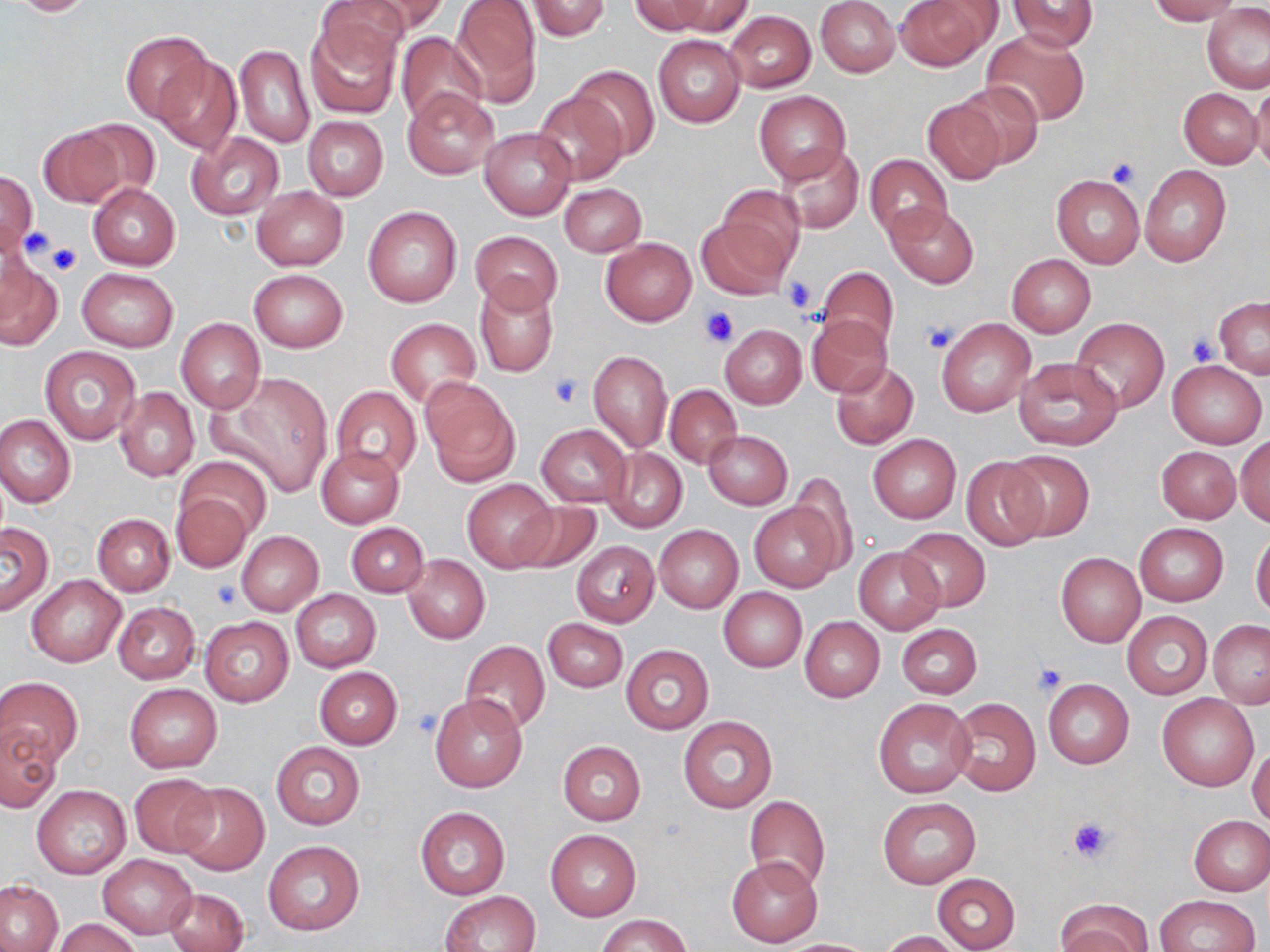
slide_level_diagnosis: no evidence of blood parasites
platelet_locations: 'approximate bounding boxes as (x1,y1)-(x2,y2) corner pairs in pixels: (1108,157)-(1141,188), (22,226)-(52,259), (47,242)-(83,276), (782,276)-(817,313), (701,306)-(740,346), (922,318)-(959,353), (1187,332)-(1219,366), (550,374)-(583,407), (213,581)-(241,609), (1033,662)-(1067,696), (411,707)-(445,737), (1066,815)-(1115,864)'
image_size: 1270×952 pixels
magnification: 1000x
uninfected_red_blood_cell_locations: 'approximate bounding boxes as (x1,y1)-(x2,y2) corner pairs in pixels: (5,0)-(101,17), (314,0)-(415,73), (351,0)-(449,41), (450,0)-(542,101), (631,0)-(712,36), (665,0)-(752,36), (816,0)-(900,77), (893,0)-(998,71), (1007,0)-(1102,52), (1148,0)-(1243,23), (526,1)-(610,41), (1202,4)-(1270,93), (725,11)-(815,93), (304,17)-(402,118), (983,29)-(1090,126), (121,30)-(212,124), (395,32)-(488,123), (654,35)-(745,126), (235,45)-(314,148), (151,54)-(242,154), (571,65)-(660,159), (1250,80)-(1270,176), (954,81)-(1045,169), (402,86)-(501,180), (1179,87)-(1261,166), (753,89)-(851,185), (533,90)-(627,186), (922,100)-(1006,184), (302,116)-(388,201), (75,118)-(161,201), (35,125)-(128,209), (480,127)-(576,220), (188,132)-(284,220), (774,143)-(865,234), (863,154)-(951,240), (1140,164)-(1231,266), (0,170)-(37,255), (1052,175)-(1144,267), (87,182)-(181,271), (558,184)-(646,256), (252,186)-(348,270), (712,186)-(806,281), (887,203)-(978,289), (362,206)-(462,308), (697,219)-(790,299), (470,230)-(562,313), (601,238)-(696,325), (0,251)-(63,352), (1007,254)-(1096,337), (816,266)-(899,350), (77,268)-(177,351), (250,269)-(347,353), (473,279)-(559,376), (1214,297)-(1269,379), (805,315)-(893,397), (176,318)-(265,412), (1070,318)-(1170,413), (386,319)-(480,405), (936,319)-(1035,416), (720,325)-(806,408), (40,345)-(140,443), (588,351)-(672,453), (1013,357)-(1122,450), (1166,360)-(1266,448), (832,361)-(919,451), (217,375)-(333,498), (421,379)-(521,486), (664,384)-(742,468), (114,387)-(199,481), (332,387)-(422,479), (0,414)-(76,508), (535,423)-(632,507), (704,430)-(792,509), (868,434)-(962,524), (1235,436)-(1270,527), (1155,444)-(1243,524), (316,446)-(404,528), (604,447)-(687,533), (1002,450)-(1094,542), (176,456)-(271,540), (961,457)-(1050,552), (787,472)-(857,569), (463,481)-(557,571), (172,493)-(251,571), (510,500)-(601,574), (750,501)-(843,593), (92,513)-(175,596), (345,521)-(428,597), (0,522)-(52,615), (1133,522)-(1229,606), (654,524)-(743,613), (898,527)-(990,612), (236,531)-(324,616), (1250,534)-(1270,621), (571,541)-(660,627), (855,546)-(944,635), (1056,553)-(1144,647), (402,554)-(490,644), (27,575)-(125,667), (719,587)-(807,672), (291,588)-(381,672), (113,602)-(201,684), (1122,611)-(1213,699), (200,616)-(295,707), (800,616)-(885,702), (543,618)-(628,692), (1208,620)-(1270,707), (895,623)-(982,699), (461,641)-(550,733), (620,644)-(714,735), (314,666)-(403,749), (1,677)-(83,769), (1043,678)-(1134,769), (124,684)-(223,772), (429,693)-(527,793), (1158,693)-(1258,791), (873,697)-(974,797), (947,698)-(1040,796), (678,716)-(777,814), (1,724)-(61,813), (558,741)-(646,825), (271,742)-(365,829), (1247,745)-(1270,827), (128,773)-(220,859), (175,782)-(268,874), (33,784)-(130,878), (743,796)-(830,892), (877,797)-(981,887), (415,806)-(510,899), (1188,815)-(1270,895), (545,830)-(641,921), (264,841)-(365,935), (97,854)-(197,939), (727,856)-(823,947), (931,872)-(1021,952), (0,880)-(62,950), (165,887)-(248,952), (442,891)-(541,952), (1155,895)-(1257,952), (1056,900)-(1153,952), (595,914)-(692,952), (54,917)-(141,952), (879,931)-(964,952), (782,938)-(880,951)'
modality: optical microscopy
stain: May-Grünwald-Giemsa
preparation: thin blood film
field_of_view: single